Name the parasite shown.
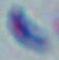

Toxoplasma gondii.

1000x magnification. Micrograph.